Classify this cell by malaria status.
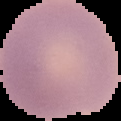
It is uninfected.

The area outside the segmented cell region is set to black. From a thin blood film. Image is 121×121 pixels.